State the preparation type.
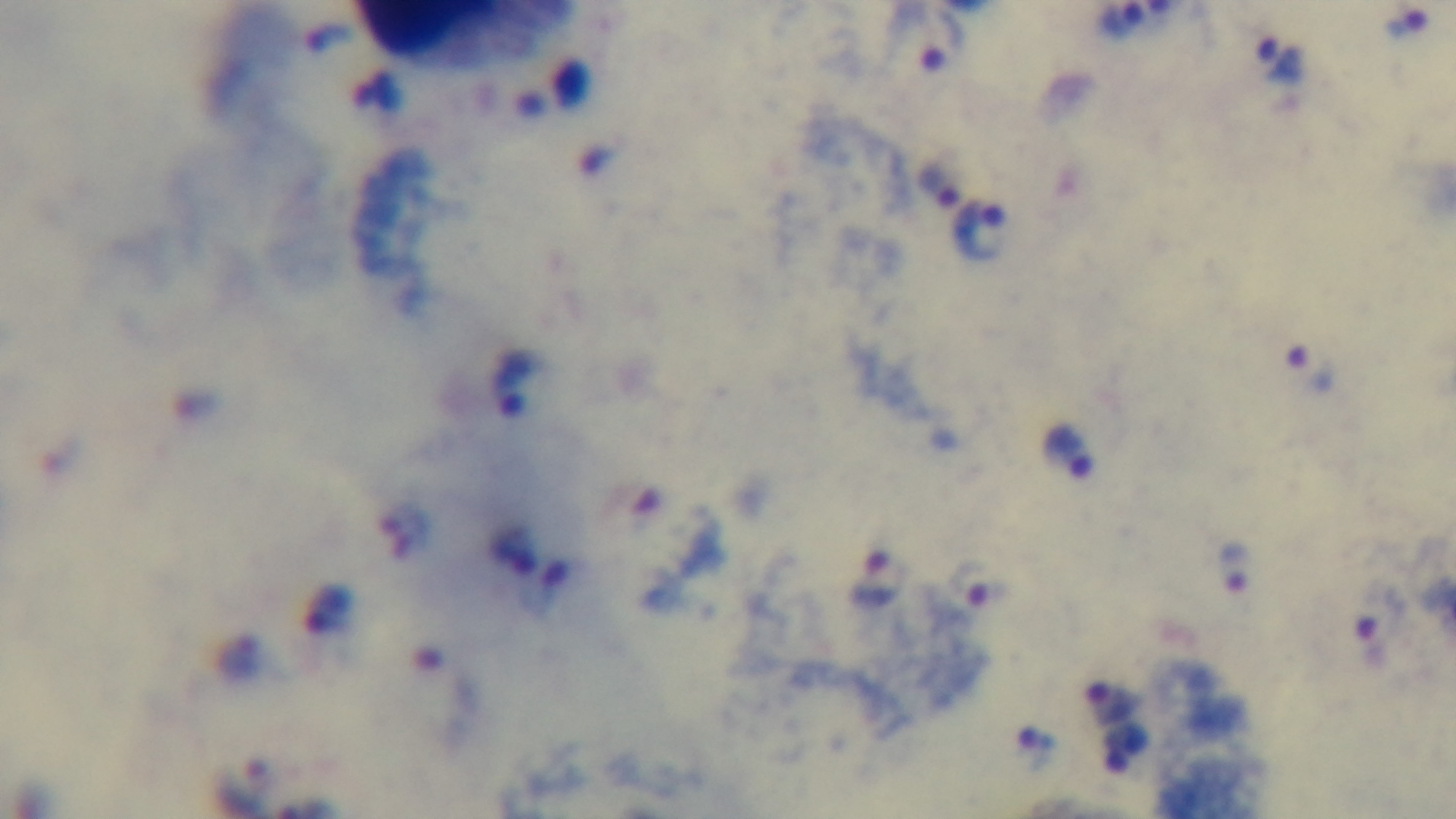

Thick.

100x oil-immersion objective. Malaria status: infected. Single field of view. Giemsa-stained. Light microscopy. Captured with a mounted 4K digital camera.